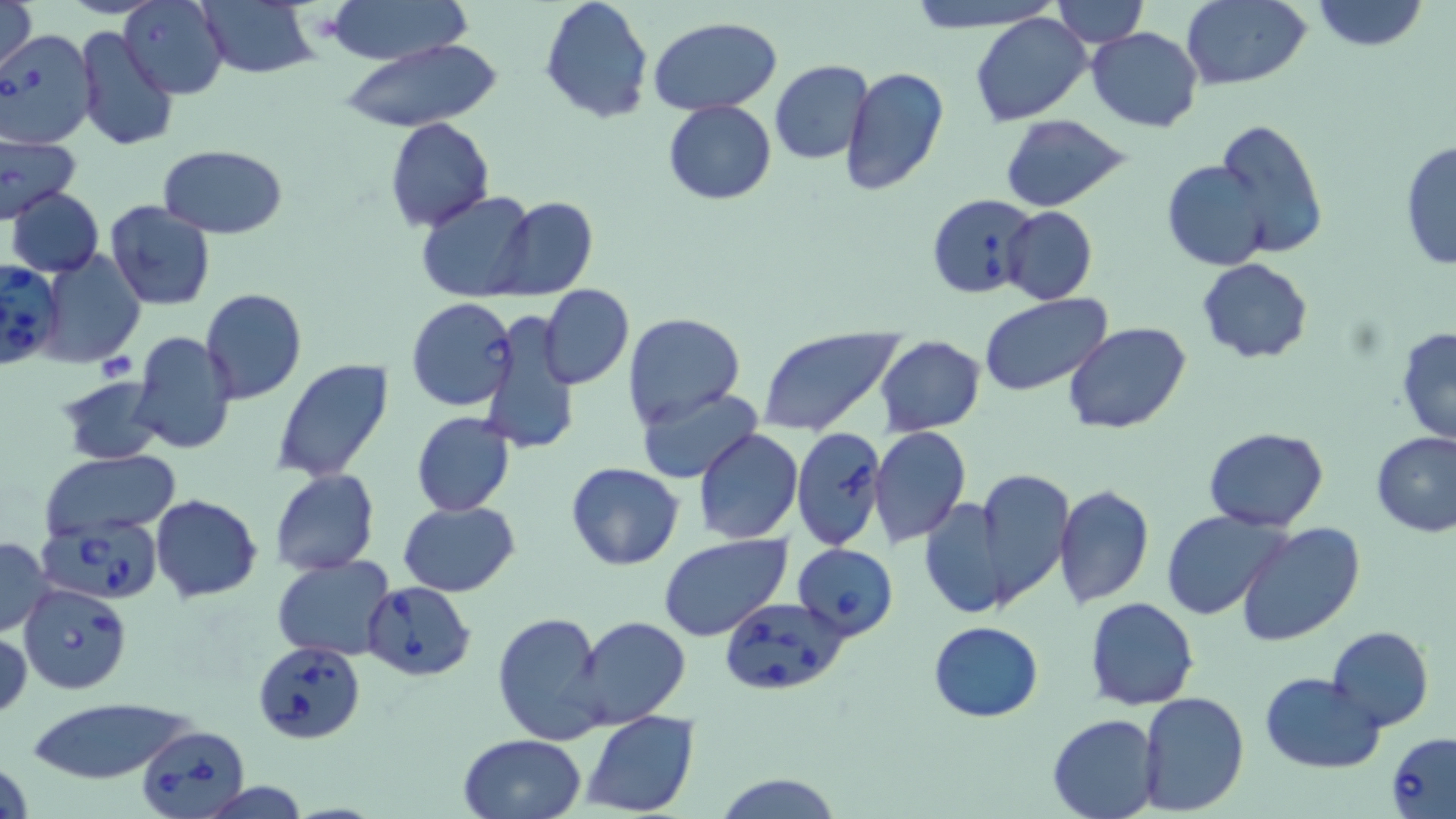

Approximate bounding boxes as (x1, y1, x2, y2) in pixels. Uninfected red blood cell locations: (1, 0, 39, 76), (321, 0, 474, 64), (538, 0, 654, 123), (899, 0, 1063, 30), (1183, 0, 1314, 90), (1311, 0, 1428, 52), (120, 1, 228, 100), (193, 1, 321, 81), (1048, 1, 1151, 47), (970, 12, 1093, 126), (648, 15, 782, 115), (74, 24, 181, 151), (1085, 27, 1204, 132), (340, 35, 504, 132), (770, 59, 875, 165), (840, 65, 951, 197), (663, 100, 777, 204), (999, 114, 1133, 212), (1211, 117, 1330, 258), (383, 118, 494, 231), (0, 131, 82, 221), (1399, 139, 1455, 270), (158, 143, 288, 238), (1163, 159, 1275, 270), (7, 187, 103, 277), (414, 190, 540, 304), (489, 196, 597, 300), (104, 200, 215, 311), (1001, 207, 1097, 305), (37, 251, 146, 367), (1195, 258, 1314, 366), (540, 284, 633, 389), (200, 288, 307, 405), (978, 293, 1112, 396), (478, 309, 581, 455), (623, 310, 746, 429), (1063, 321, 1192, 435), (1396, 325, 1456, 446), (756, 327, 903, 436), (129, 330, 239, 455), (875, 336, 986, 436), (270, 357, 396, 483), (57, 376, 165, 467), (636, 389, 760, 480), (410, 411, 516, 516), (1204, 426, 1329, 530), (870, 427, 970, 547), (694, 429, 803, 544), (1372, 432, 1456, 537), (38, 451, 182, 541), (566, 462, 684, 569), (269, 470, 379, 575), (964, 470, 1077, 610), (1054, 485, 1154, 609), (150, 494, 262, 604), (917, 498, 1013, 622), (397, 500, 522, 597), (1163, 510, 1287, 619), (1235, 522, 1367, 647), (658, 534, 790, 642), (0, 535, 54, 637), (273, 556, 398, 659), (1085, 597, 1198, 711), (492, 609, 610, 746), (573, 617, 690, 729), (928, 621, 1043, 723), (1326, 626, 1433, 731), (1, 629, 31, 723), (1261, 672, 1384, 772), (1138, 691, 1249, 813), (24, 695, 195, 786), (581, 710, 701, 818), (1048, 713, 1160, 818), (459, 734, 587, 819), (1, 753, 32, 819), (713, 772, 844, 819), (199, 780, 312, 818). Babesia divergens-infected red blood cell locations: (0, 29, 98, 149), (926, 192, 1035, 301), (1, 262, 65, 369), (407, 297, 519, 412), (791, 428, 886, 551), (37, 514, 165, 603), (793, 543, 899, 638), (362, 580, 476, 681), (18, 582, 132, 694), (720, 595, 849, 696), (254, 639, 366, 743), (136, 722, 252, 818), (1387, 732, 1456, 818). Slide-level diagnosis: Babesia divergens. Image is 1456×819 pixels. Single field of view. May-Grünwald-Giemsa-stained preparation. Light microscopy. Thin blood film. Captured at 1000x magnification.